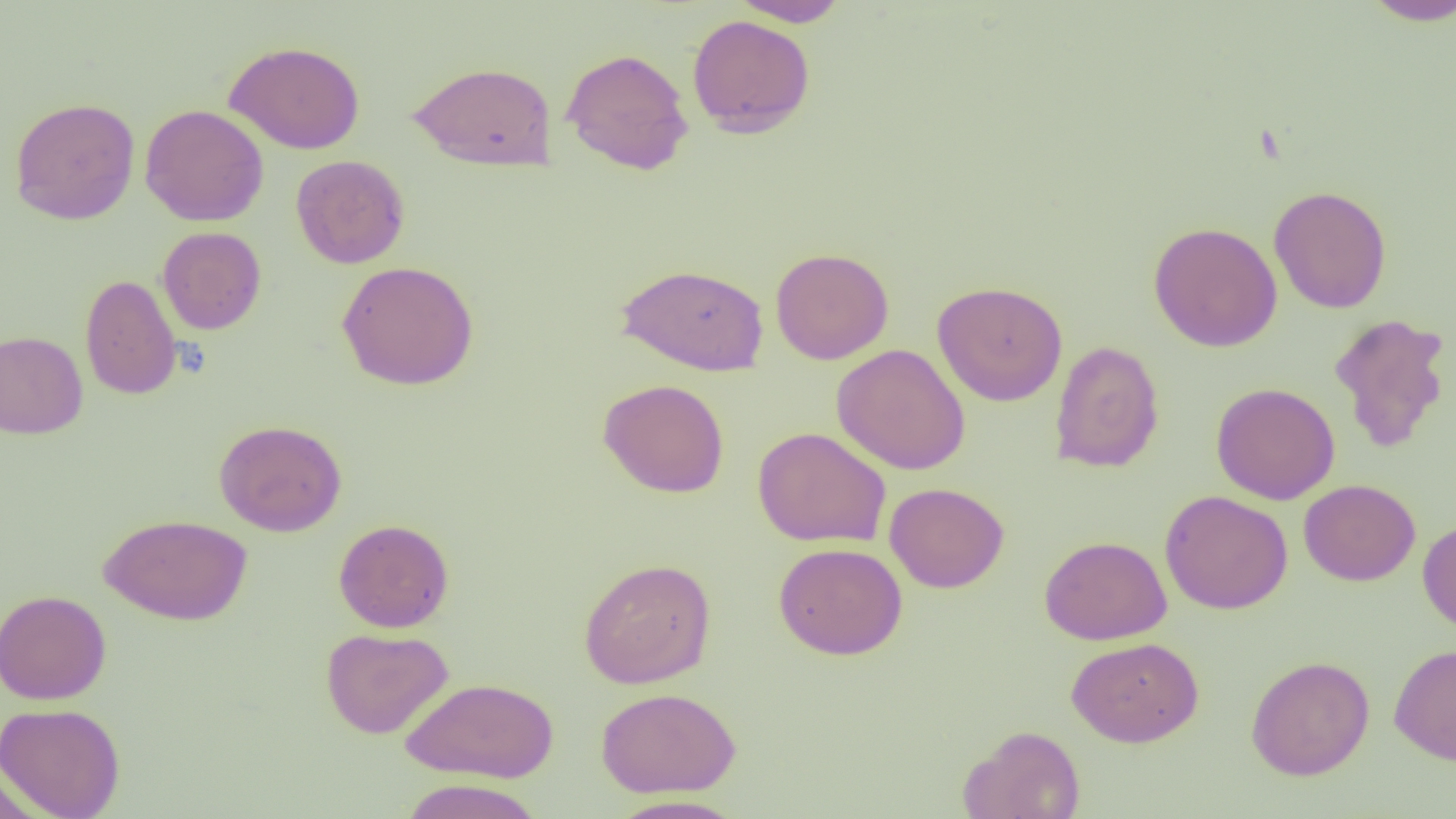 Approximate bounding boxes as (x1,y1)-(x2,y2) corner pairs in pixels. Uninfected red blood cell locations: (729,0)-(851,27), (1359,0)-(1456,26), (687,14)-(816,138), (224,40)-(365,154), (561,47)-(694,175), (408,61)-(558,171), (10,97)-(140,225), (140,104)-(268,227), (291,155)-(409,269), (1269,185)-(1392,313), (1148,222)-(1283,352), (157,226)-(266,334), (770,247)-(894,364), (337,261)-(478,390), (615,262)-(769,375), (80,274)-(182,400), (932,281)-(1068,406), (1329,312)-(1452,453), (0,330)-(88,439), (1049,340)-(1164,473), (832,343)-(970,475), (598,378)-(730,498), (1211,382)-(1340,505), (214,419)-(347,537), (753,426)-(891,548), (1299,479)-(1421,586), (885,482)-(1009,593), (1160,490)-(1293,614), (99,513)-(252,626), (333,518)-(454,633), (1417,518)-(1456,636), (1040,535)-(1172,644), (773,542)-(907,660), (578,557)-(716,688), (0,589)-(112,705), (321,627)-(453,739), (1066,637)-(1204,747), (1389,643)-(1456,765), (1245,656)-(1375,780), (401,677)-(559,783), (596,687)-(741,798), (0,702)-(126,818), (961,725)-(1087,819), (0,763)-(44,819), (399,778)-(545,819), (606,794)-(749,819). Slide-level diagnosis: negative for blood parasites. Thin blood smear. 1000x magnification. Optical microscopy. Single field of view. Image is 1456×819 pixels.